Outline each Plasmodium falciparum-infected red blood cell.
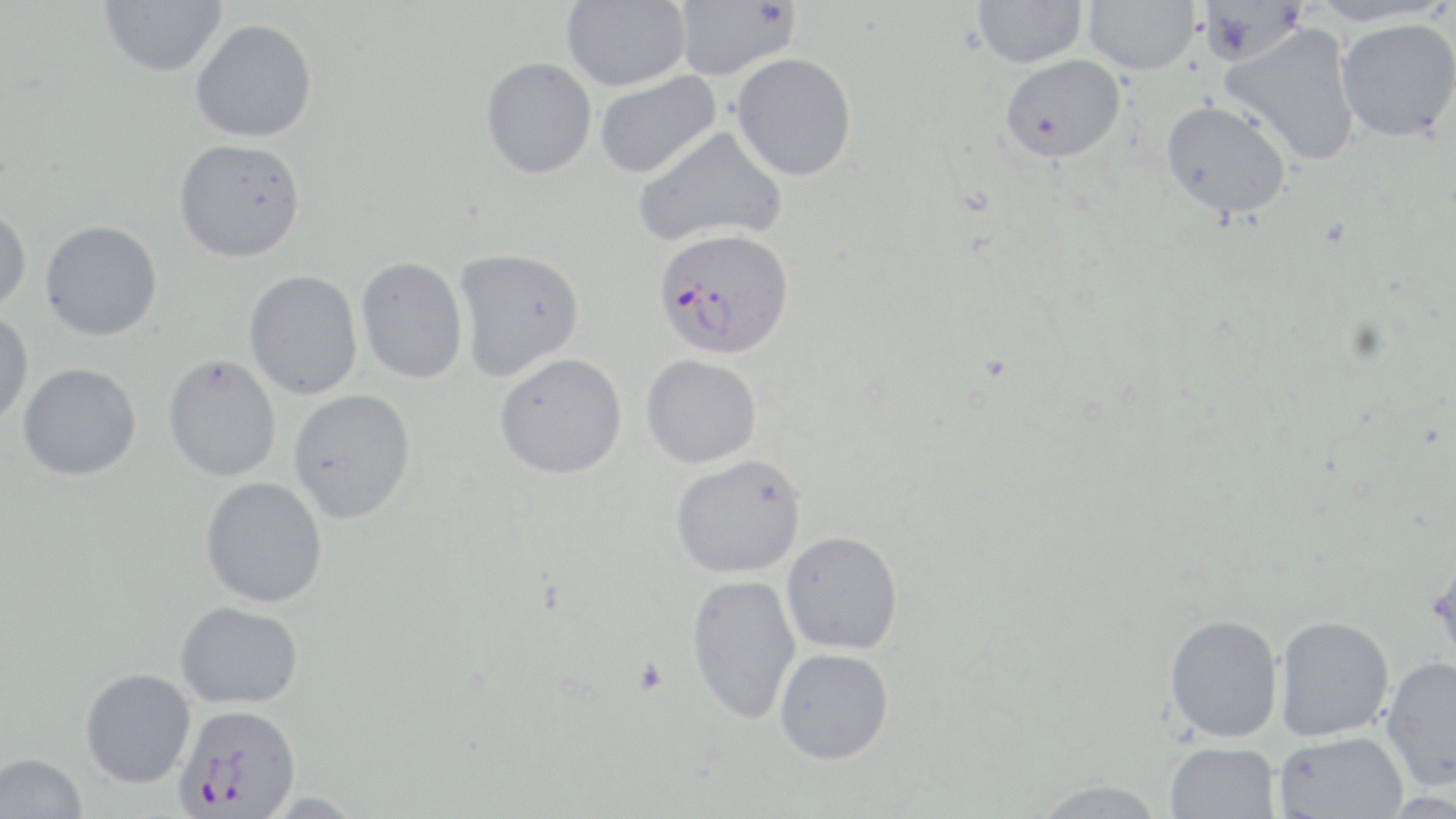
Approximate bounding boxes as (x1,y1)-(x2,y2) corner pairs in pixels.
Plasmodium falciparum-infected red blood cells: (654,227)-(794,359), (173,704)-(301,817).

{
  "slide_level_diagnosis": "Plasmodium falciparum",
  "magnification": "1000x",
  "field_of_view": "one of a larger specimen",
  "stain": "May-Grünwald-Giemsa",
  "image_size": "1456×819 pixels",
  "modality": "optical microscopy",
  "uninfected_red_blood_cell_locations": "approximate bounding boxes as (x1,y1)-(x2,y2) corner pairs in pixels: (98,0)-(227,77), (561,0)-(690,91), (673,0)-(802,80), (1083,0)-(1200,75), (973,1)-(1087,69), (1196,1)-(1309,68), (190,18)-(317,143), (1336,18)-(1455,143), (1220,23)-(1361,166), (731,53)-(857,181), (1000,54)-(1126,162), (480,57)-(597,179), (593,71)-(722,179), (1160,100)-(1291,219), (633,126)-(788,250), (173,137)-(307,263), (0,205)-(31,313), (40,220)-(163,341), (453,248)-(585,381), (356,256)-(469,384), (244,270)-(363,400), (0,309)-(35,429), (495,353)-(627,479), (163,354)-(282,483), (641,355)-(762,468), (18,363)-(142,481), (288,389)-(416,524), (671,453)-(807,579), (200,476)-(328,608), (781,530)-(904,655), (686,573)-(801,725), (175,602)-(304,709), (1164,613)-(1283,742), (1274,615)-(1394,742), (775,648)-(894,764), (1381,655)-(1456,791), (80,668)-(196,789), (1273,731)-(1407,819), (1164,742)-(1281,819), (0,752)-(87,819), (1031,779)-(1170,818)",
  "preparation": "thin blood film"
}